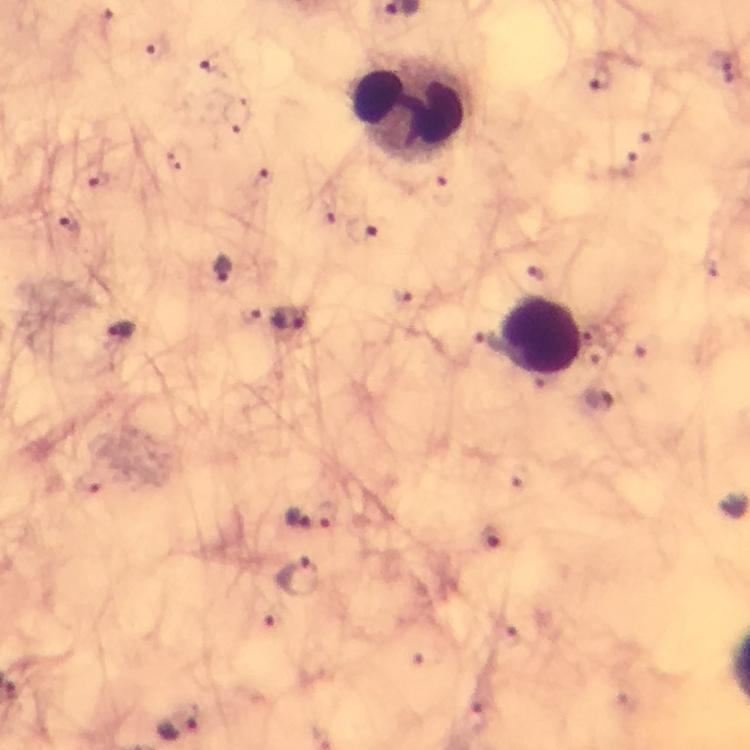

image_size: 750×750 pixels
stain: Giemsa
context: from a malaria diagnostic workup
cropped_from: one field of view
immersion_oil: used
capture: smartphone photograph through a microscope
preparation: thick smear
magnification: 100x
leukocyte_locations: 'approximate centers as {x, y} in pixels: {414, 112}, {540, 334}'
malaria_parasite_locations: 'approximate centers as {x, y} in pixels: {157, 52}, {600, 79}, {70, 224}, {222, 268}, {293, 319}, {122, 330}, {294, 514}, {328, 515}, {493, 542}, {300, 576}, {181, 724}'